Describe the morphology of the erythrocytes.
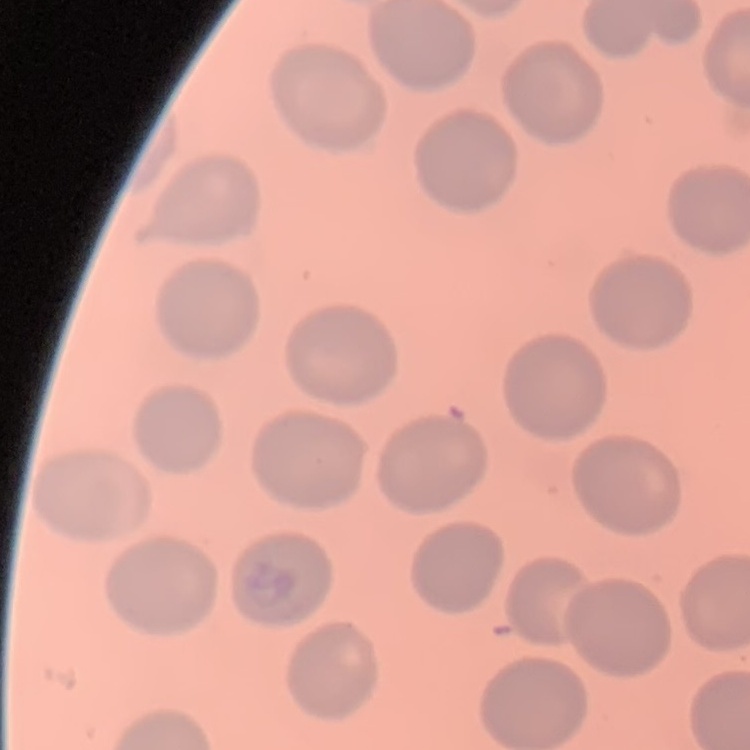
No rouleaux formation.

Summary:
  - Stain: Field's or Giemsa
  - Preparation: thin blood smear
  - Image type: square crop of a larger photomicrograph